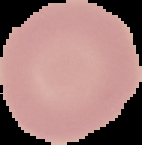

preparation = thin blood film
image size = 142×145 pixels
result = no Plasmodium parasites seen
image type = cell region segmented out of the field of view; surrounding area masked to black